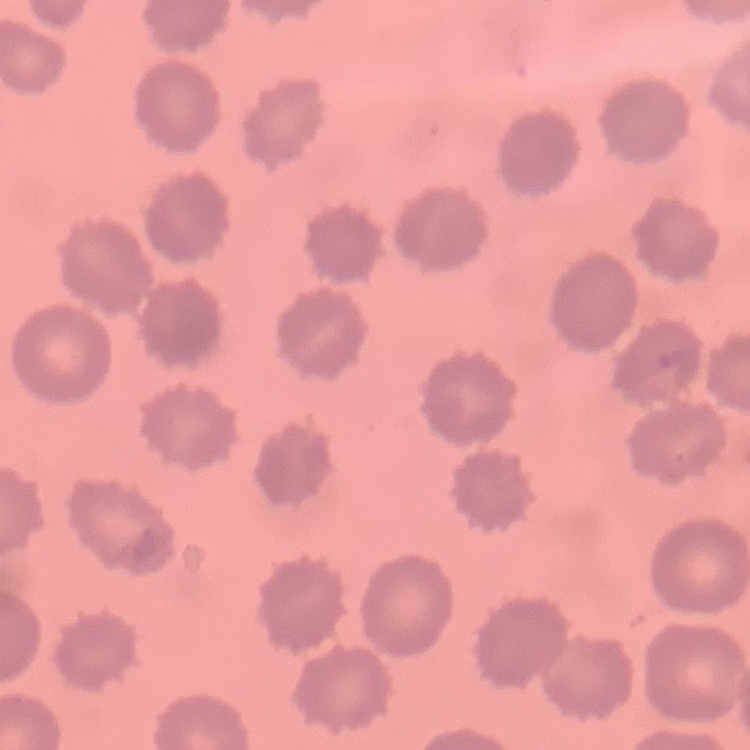
red blood cell morphology = no rouleaux formation
image type = one tile cut from a larger photomicrograph
preparation = thin peripheral smear
stain = Field's or Giemsa